Assess this cell for malaria.
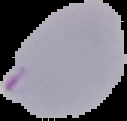
It is parasitized.

Summary:
  - Preparation: thin blood film
  - Image size: 127×121 pixels
  - Image type: segmented cell region with the area outside set to black